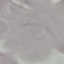
result: no malaria parasites detected
capture: smartphone camera at the microscope eyepiece
preparation: thin blood smear
stain: Giemsa
image_type: cell patch, automatically extracted from a larger field of view and resized to 64 × 64 pixels